Draw a bounding box around every malaria parasite.
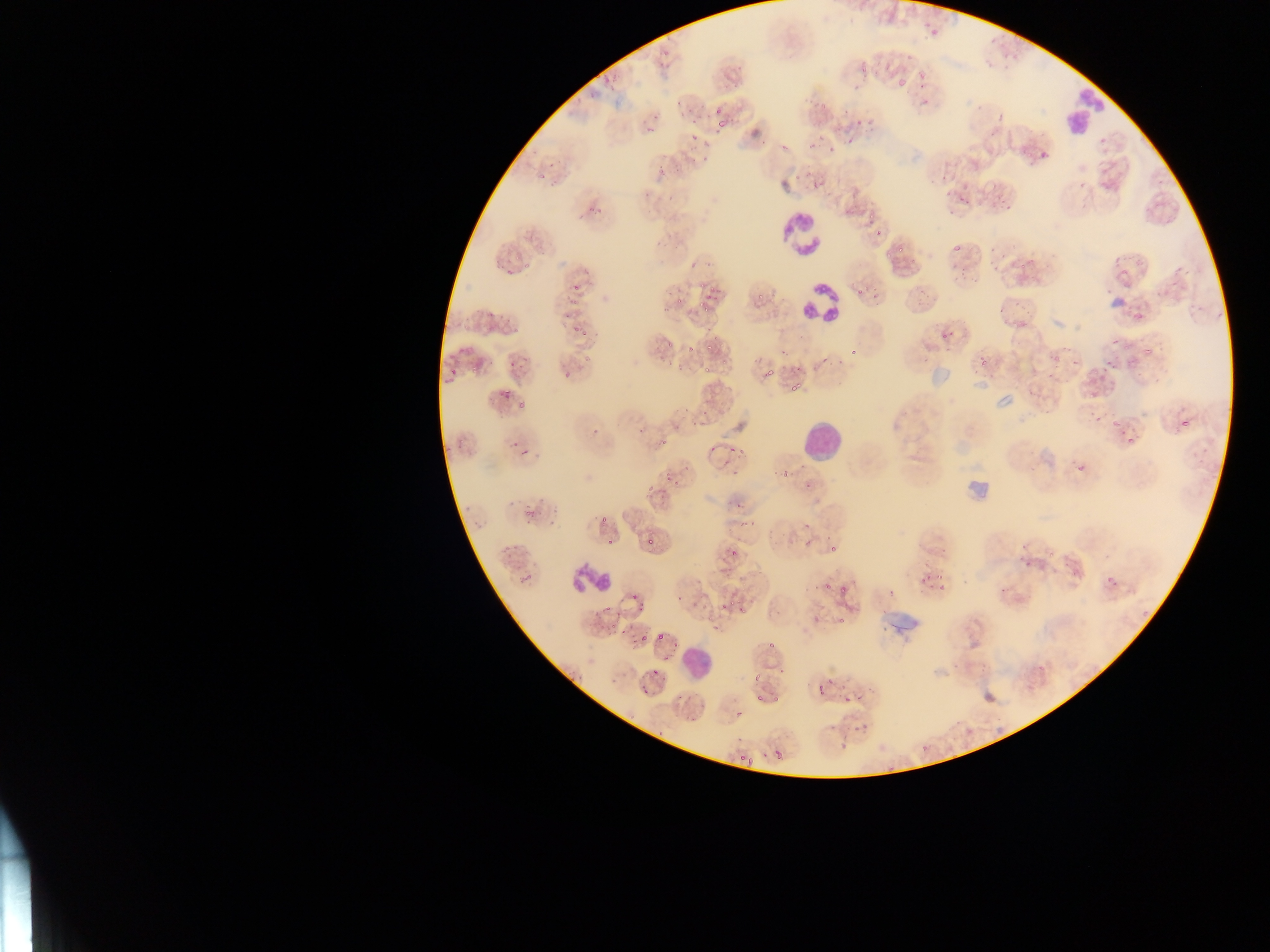

Approximate bounding boxes as [left, top, right, bottom] in pixels.
Malaria parasites: [921, 15, 950, 41], [855, 54, 871, 75], [880, 67, 888, 75], [897, 70, 916, 92], [916, 71, 931, 84], [709, 102, 728, 129], [679, 106, 695, 119], [714, 115, 734, 134], [853, 121, 862, 128], [647, 125, 656, 134], [687, 126, 705, 141], [804, 132, 823, 155], [845, 138, 862, 148], [776, 139, 793, 154], [698, 144, 713, 158], [825, 149, 833, 157], [1033, 152, 1046, 162], [538, 159, 556, 178], [807, 168, 828, 193], [651, 171, 674, 183], [995, 193, 1007, 205], [957, 196, 969, 209], [591, 205, 600, 214], [875, 228, 883, 238], [896, 243, 909, 253], [951, 245, 965, 255], [688, 250, 709, 269], [982, 250, 1005, 273], [503, 261, 521, 278], [953, 266, 970, 285], [1161, 267, 1180, 296], [1113, 274, 1127, 288], [851, 280, 874, 302], [571, 284, 583, 294], [908, 289, 930, 307], [696, 293, 714, 316], [754, 295, 763, 305], [996, 302, 1015, 325], [1124, 307, 1145, 327], [486, 308, 500, 325], [559, 309, 576, 322], [570, 326, 580, 334], [938, 326, 961, 341], [581, 332, 591, 338], [1107, 340, 1119, 352], [706, 341, 716, 356], [685, 345, 694, 353], [1142, 345, 1155, 357], [661, 346, 673, 361], [848, 346, 858, 356], [976, 349, 990, 366], [1047, 350, 1060, 373], [815, 354, 824, 371], [508, 359, 519, 372], [1102, 360, 1114, 375], [449, 361, 459, 378], [468, 363, 478, 376], [793, 363, 801, 380], [762, 366, 773, 381], [699, 369, 710, 375], [562, 372, 570, 380], [789, 379, 807, 396], [500, 385, 511, 401], [514, 390, 536, 408], [691, 410, 709, 428], [1085, 410, 1103, 426], [1178, 415, 1188, 427], [1110, 417, 1126, 432], [634, 425, 651, 438], [591, 428, 600, 436], [656, 431, 677, 447], [1127, 434, 1135, 444], [729, 442, 740, 453], [707, 445, 718, 458], [516, 453, 531, 463], [719, 458, 735, 472], [1073, 461, 1086, 475], [778, 464, 790, 475], [662, 470, 677, 484], [801, 475, 818, 494], [647, 481, 657, 493], [656, 484, 671, 496], [732, 494, 749, 516], [521, 505, 538, 520], [801, 507, 819, 532], [598, 509, 617, 525], [499, 534, 524, 553], [645, 534, 658, 550], [603, 537, 617, 548], [827, 540, 840, 552], [798, 541, 808, 547], [728, 543, 741, 558], [1017, 552, 1031, 571], [1061, 552, 1074, 566], [1102, 566, 1118, 591], [917, 568, 933, 588], [519, 573, 533, 585], [934, 573, 945, 580], [821, 578, 835, 592], [938, 582, 951, 592], [836, 587, 844, 595], [886, 587, 898, 595], [999, 587, 1007, 595], [736, 597, 749, 614], [633, 598, 654, 614], [715, 604, 727, 618], [600, 607, 610, 617], [836, 610, 849, 627], [603, 625, 628, 639], [658, 630, 668, 643], [639, 631, 651, 645], [766, 633, 782, 652], [663, 649, 678, 662], [951, 654, 968, 671], [747, 667, 761, 684], [651, 668, 664, 682], [771, 686, 785, 703], [842, 687, 854, 704], [641, 688, 649, 695], [754, 688, 765, 705], [733, 708, 744, 719], [851, 713, 881, 736], [920, 740, 932, 752], [772, 744, 789, 763], [739, 753, 747, 760], [746, 757, 760, 767] | approximate [x, y] pixel centers of objects too small to bound: [924, 102], [820, 688], [661, 734], [844, 747].

Summary:
  - Leukocyte locations: [1057, 77, 1117, 136], [778, 211, 825, 259], [791, 211, 836, 300], [798, 283, 839, 321], [801, 421, 841, 461], [569, 563, 612, 596], [684, 646, 712, 675]
  - Artifact (stain precipitate or debris) locations: [962, 460, 998, 508], [874, 612, 924, 641]
  - Preparation: thin blood film
  - Image size: 1270×952 pixels
  - Capture: mobile-phone photograph through a microscope
  - Country: Ghana
  - Field of view: single